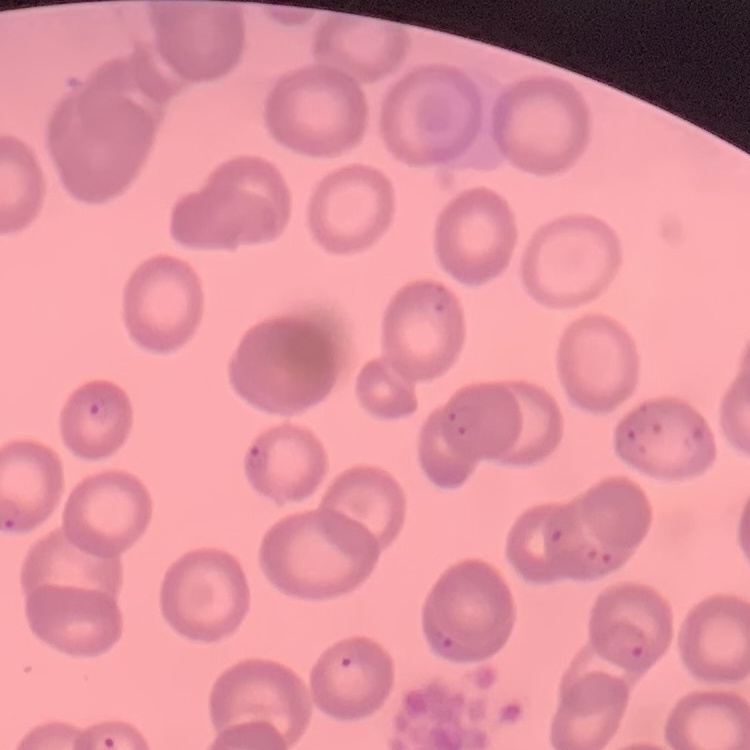

{
  "red_blood_cell_morphology": "no rouleaux formation",
  "preparation": "thin blood film",
  "stain": "Field's or Giemsa",
  "image_type": "one tile cut from a larger photomicrograph"
}